Assess this cell for malaria.
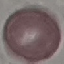

Uninfected.

Acquired by smartphone through the microscope eyepiece. Giemsa stain. Cell patch, automatically extracted from a larger field of view and resized to 64 × 64 pixels. Thin blood film.